Name the blood parasite species.
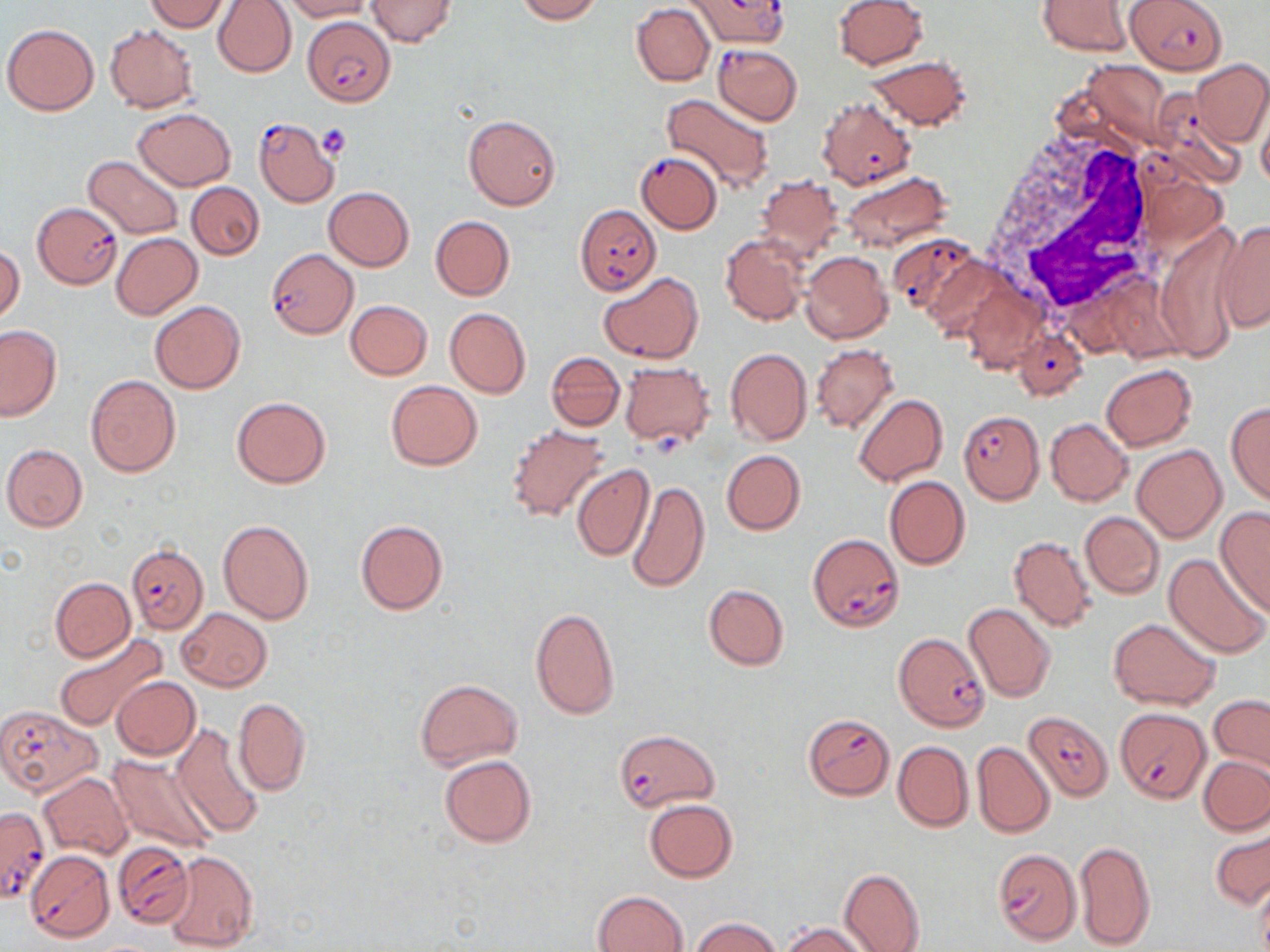
Plasmodium falciparum.

{
  "modality": "light microscopy",
  "image_size": "1270×952 pixels",
  "uninfected_red_blood_cell_locations": "approximate bounding boxes as (x1,y1)-(x2,y2) corner pairs in pixels: (146,0)-(230,32), (214,0)-(297,76), (282,0)-(372,20), (367,0)-(457,45), (515,0)-(603,23), (834,0)-(928,69), (1036,1)-(1135,57), (631,3)-(714,86), (3,23)-(99,116), (104,23)-(198,113), (868,56)-(972,131), (1078,59)-(1173,149), (1191,59)-(1270,147), (662,93)-(775,194), (1256,105)-(1270,189), (133,108)-(237,190), (463,114)-(562,210), (98,152)-(191,318), (83,154)-(186,240), (840,171)-(952,253), (754,175)-(844,264), (188,183)-(263,259), (324,187)-(414,270), (431,215)-(514,301), (1216,220)-(1270,334), (1154,224)-(1246,362), (111,233)-(202,319), (721,233)-(810,326), (1,244)-(25,324), (800,252)-(893,344), (963,279)-(1046,375), (344,300)-(433,380), (150,301)-(245,393), (444,308)-(530,398), (0,325)-(61,420), (811,344)-(899,435), (725,348)-(811,446), (545,352)-(625,431), (620,362)-(715,448), (1101,364)-(1197,451), (85,375)-(180,476), (385,381)-(483,470), (852,395)-(948,486), (232,397)-(331,487), (1226,401)-(1270,506), (1046,418)-(1132,506), (506,425)-(611,522), (2,444)-(89,532), (1132,444)-(1226,543), (721,450)-(806,535), (571,464)-(655,562), (884,475)-(969,570), (627,480)-(709,593), (1214,506)-(1270,617), (1079,512)-(1165,599), (218,519)-(314,623), (355,519)-(448,615), (1008,535)-(1098,632), (1164,553)-(1269,661), (50,577)-(135,662), (702,584)-(789,671), (963,603)-(1057,704), (530,606)-(620,720), (177,608)-(272,690), (1108,618)-(1221,709), (54,632)-(168,732), (111,676)-(200,759), (414,678)-(524,770), (1209,694)-(1270,775), (232,698)-(310,796), (169,723)-(267,841), (892,740)-(973,832), (971,742)-(1054,838), (438,753)-(537,849), (1200,756)-(1270,834), (109,757)-(222,854), (39,772)-(134,861), (643,798)-(738,881), (1210,825)-(1270,913), (1075,840)-(1156,950), (163,849)-(259,952), (838,867)-(924,952), (1253,877)-(1270,952), (594,890)-(689,952), (690,917)-(780,952), (782,922)-(873,952)",
  "magnification": "1000x",
  "field_of_view": "single",
  "stain": "May-Grünwald-Giemsa",
  "plasmodium_falciparum_infected_red_blood_cell_locations": "approximate bounding boxes as (x1,y1)-(x2,y2) corner pairs in pixels: (688,0)-(790,50), (1125,0)-(1228,74), (303,17)-(396,105), (712,44)-(802,125), (1147,89)-(1244,185), (818,96)-(915,189), (254,118)-(340,207), (636,151)-(723,233), (33,201)-(122,288), (575,203)-(661,294), (891,232)-(984,318), (266,248)-(359,338), (599,272)-(703,363), (1012,327)-(1087,401), (959,410)-(1043,503), (808,533)-(905,631), (126,544)-(208,633), (896,632)-(998,731), (0,705)-(103,797), (1117,708)-(1210,803), (1025,710)-(1110,799), (803,713)-(895,800), (612,728)-(719,811), (0,804)-(49,903), (113,842)-(194,929), (991,848)-(1081,946), (25,849)-(114,942)",
  "platelet_locations": "approximate bounding boxes as (x1,y1)-(x2,y2) corner pairs in pixels: (318,123)-(351,161)",
  "preparation": "thin blood film",
  "white_blood_cell_locations": "approximate bounding boxes as (x1,y1)-(x2,y2) corner pairs in pixels: (981,122)-(1164,322)"
}